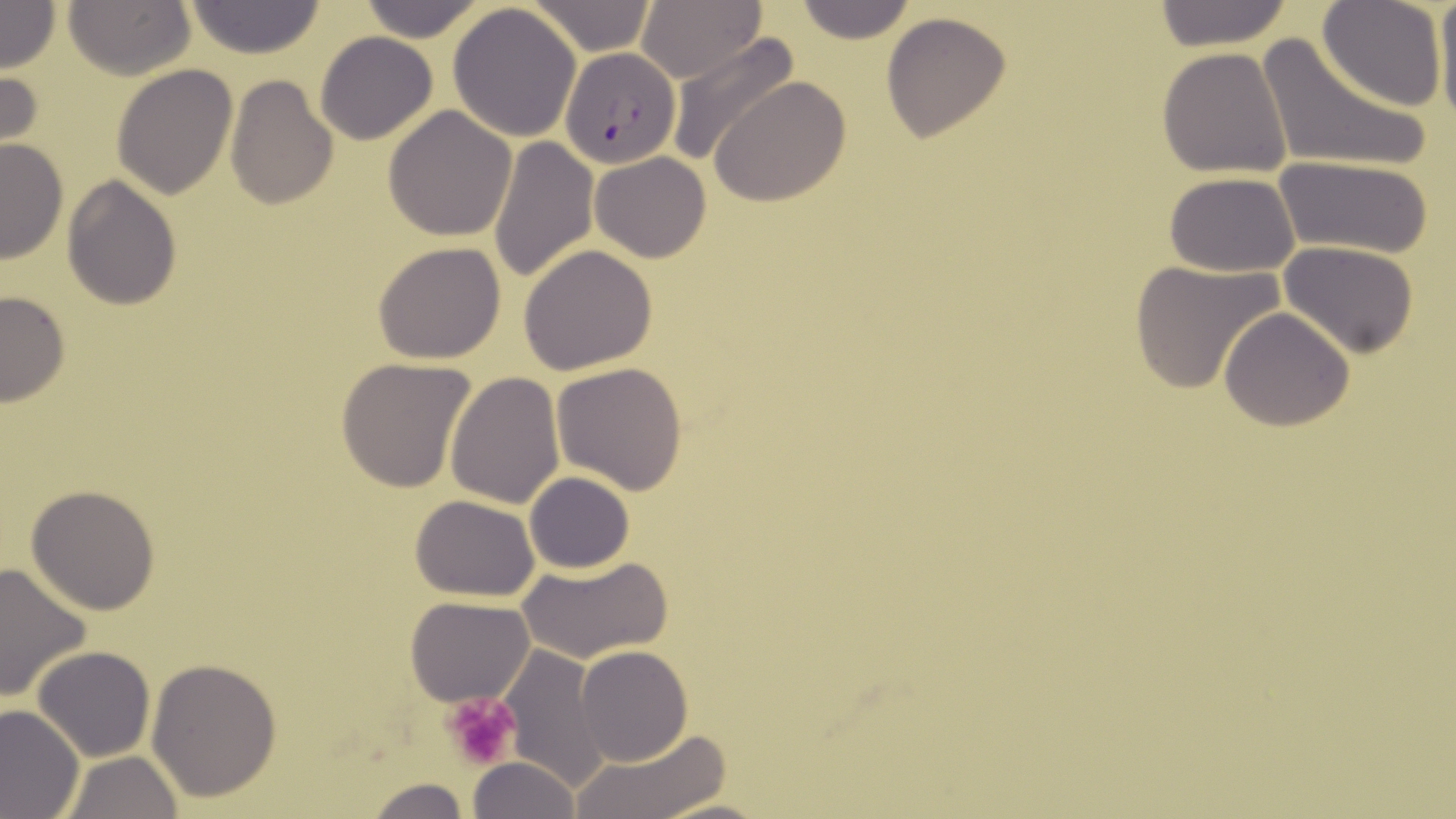
slide-level diagnosis = Plasmodium falciparum
uninfected red blood cell locations = approximate bounding boxes as named x1/y1/x2/y2 corners in pixels: (x1=63, y1=0, x2=194, y2=79), (x1=354, y1=0, x2=487, y2=42), (x1=528, y1=0, x2=657, y2=55), (x1=636, y1=0, x2=766, y2=85), (x1=790, y1=0, x2=917, y2=44), (x1=1318, y1=0, x2=1447, y2=112), (x1=1435, y1=0, x2=1456, y2=134), (x1=0, y1=1, x2=60, y2=74), (x1=184, y1=2, x2=327, y2=58), (x1=447, y1=2, x2=583, y2=143), (x1=1150, y1=2, x2=1299, y2=48), (x1=881, y1=12, x2=1013, y2=143), (x1=666, y1=30, x2=800, y2=169), (x1=314, y1=31, x2=438, y2=145), (x1=1254, y1=34, x2=1432, y2=176), (x1=1157, y1=48, x2=1293, y2=178), (x1=111, y1=63, x2=238, y2=199), (x1=0, y1=65, x2=43, y2=159), (x1=224, y1=76, x2=338, y2=210), (x1=711, y1=77, x2=852, y2=207), (x1=383, y1=106, x2=516, y2=242), (x1=487, y1=134, x2=599, y2=286), (x1=1, y1=138, x2=67, y2=265), (x1=590, y1=151, x2=712, y2=261), (x1=1272, y1=153, x2=1434, y2=261), (x1=1162, y1=172, x2=1301, y2=275), (x1=61, y1=175, x2=182, y2=309), (x1=373, y1=241, x2=507, y2=364), (x1=1279, y1=241, x2=1421, y2=358), (x1=517, y1=244, x2=659, y2=374), (x1=1127, y1=259, x2=1285, y2=394), (x1=0, y1=290, x2=71, y2=409), (x1=1218, y1=308, x2=1355, y2=431), (x1=335, y1=356, x2=478, y2=491), (x1=551, y1=362, x2=688, y2=493), (x1=444, y1=371, x2=564, y2=508), (x1=524, y1=471, x2=636, y2=574), (x1=26, y1=485, x2=160, y2=615), (x1=410, y1=495, x2=541, y2=602), (x1=516, y1=556, x2=673, y2=665), (x1=0, y1=560, x2=94, y2=704), (x1=404, y1=594, x2=535, y2=706), (x1=32, y1=645, x2=155, y2=763), (x1=498, y1=645, x2=610, y2=793), (x1=575, y1=646, x2=691, y2=765), (x1=146, y1=659, x2=283, y2=801), (x1=0, y1=704, x2=84, y2=819), (x1=572, y1=731, x2=731, y2=819), (x1=59, y1=751, x2=183, y2=819), (x1=467, y1=755, x2=580, y2=819), (x1=363, y1=776, x2=469, y2=819), (x1=655, y1=797, x2=775, y2=818)
Plasmodium falciparum-infected red blood cell locations = approximate bounding boxes as named x1/y1/x2/y2 corners in pixels: (x1=559, y1=45, x2=683, y2=169)
modality = optical microscopy
magnification = 1000x
platelet locations = approximate bounding boxes as named x1/y1/x2/y2 corners in pixels: (x1=443, y1=692, x2=519, y2=769)
field of view = single
stain = May-Grünwald-Giemsa
image size = 1456×819 pixels
preparation = thin blood film